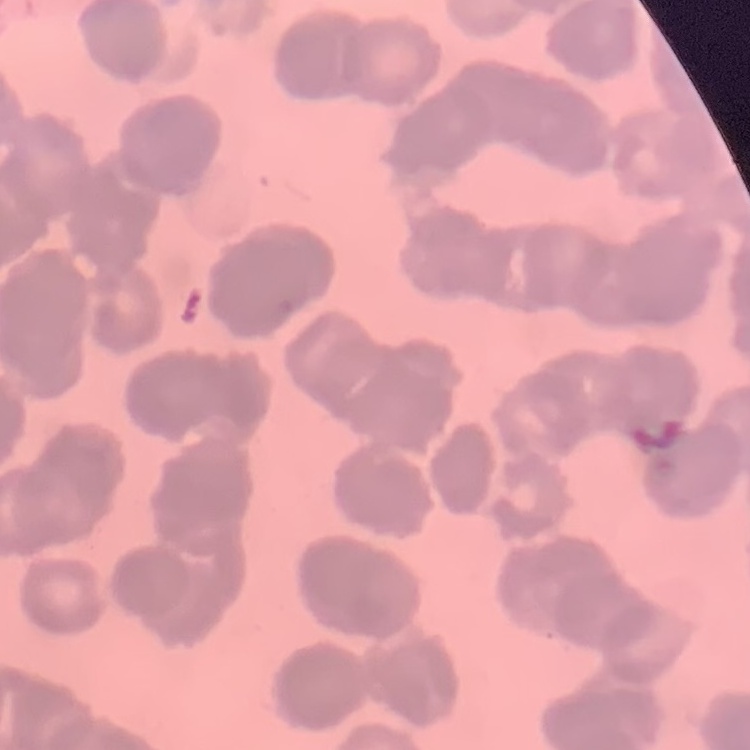
Summary:
  - Erythrocyte morphology: rouleaux formation
  - Preparation: thin blood smear
  - Image type: one tile cut from a larger photomicrograph
  - Stain: Field's or Giemsa